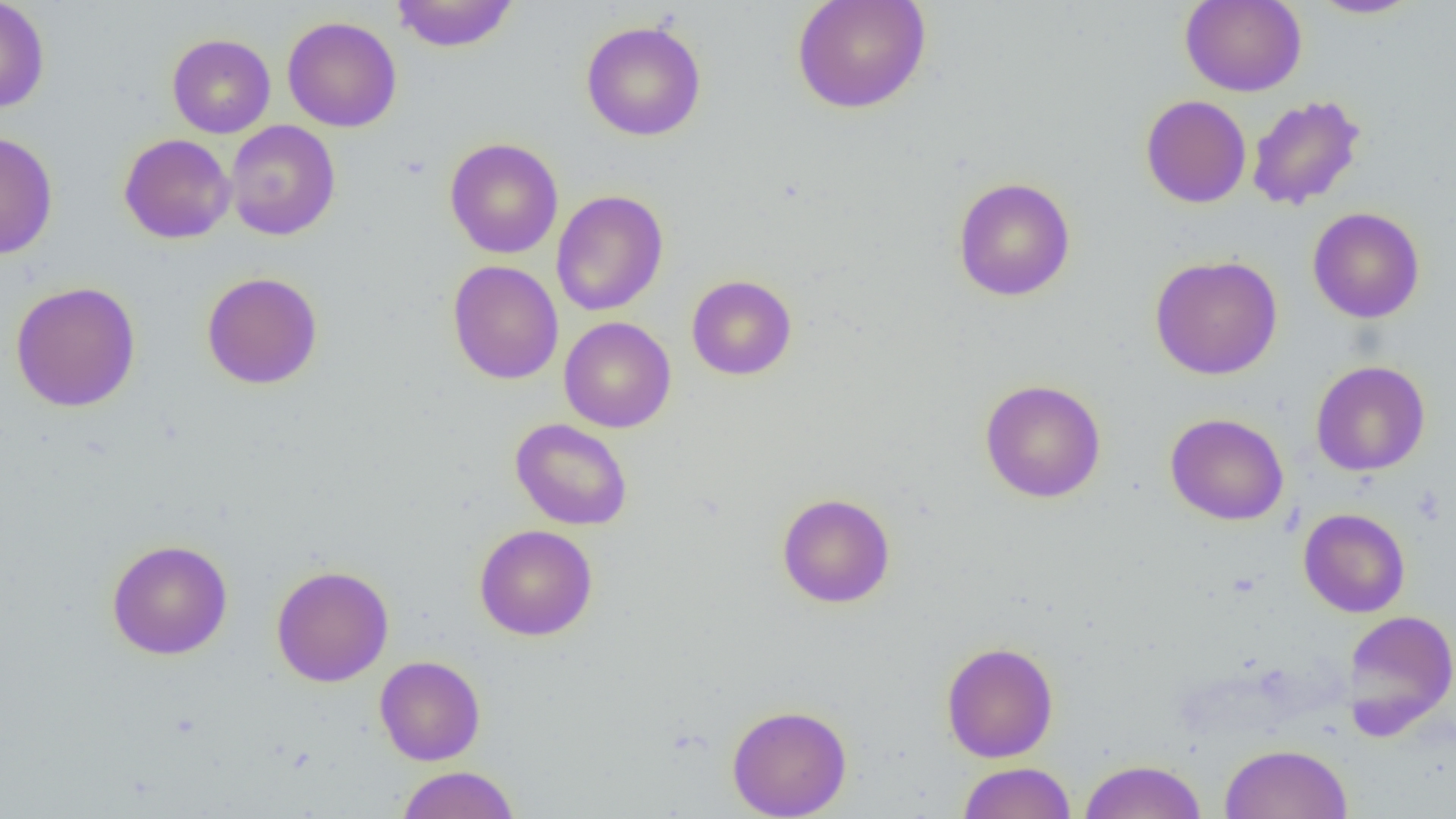
Summary:
  - Coordinate format: approximate bounding boxes as (x1, y1, x2, y2) in pixels
  - Uninfected red blood cell locations: (0, 0, 50, 114), (791, 0, 931, 115), (1179, 0, 1307, 97), (1308, 0, 1424, 19), (390, 1, 519, 52), (282, 16, 402, 132), (581, 20, 707, 141), (166, 33, 276, 138), (1246, 94, 1365, 210), (1141, 95, 1252, 208), (224, 120, 341, 241), (0, 130, 58, 260), (119, 133, 236, 244), (444, 138, 563, 259), (952, 176, 1076, 302), (551, 190, 668, 317), (1308, 207, 1425, 323), (1149, 255, 1283, 380), (447, 260, 563, 385), (202, 271, 323, 390), (686, 275, 797, 380), (10, 281, 141, 412), (559, 316, 676, 433), (1310, 360, 1431, 477), (979, 379, 1107, 503), (1165, 412, 1289, 525), (510, 418, 633, 531), (777, 492, 895, 608), (1298, 508, 1411, 617), (474, 523, 598, 641), (106, 539, 233, 660), (271, 564, 394, 687), (1341, 609, 1456, 734), (940, 641, 1059, 762), (374, 655, 486, 765), (726, 704, 852, 819), (1219, 743, 1353, 819), (1077, 759, 1207, 819), (957, 762, 1076, 819), (396, 765, 520, 819)
  - Slide-level diagnosis: negative for blood parasites
  - Field of view: single
  - Image size: 1456×819 pixels
  - Modality: optical microscopy
  - Magnification: 1000x
  - Preparation: thin blood smear